Classify this cell by malaria status.
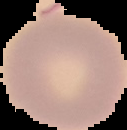
It is uninfected.

{
  "image_type": "cell region segmented out of the field of view; surrounding area masked to black",
  "preparation": "thin blood film",
  "image_size": "127×130 pixels"
}